Identify the preparation type.
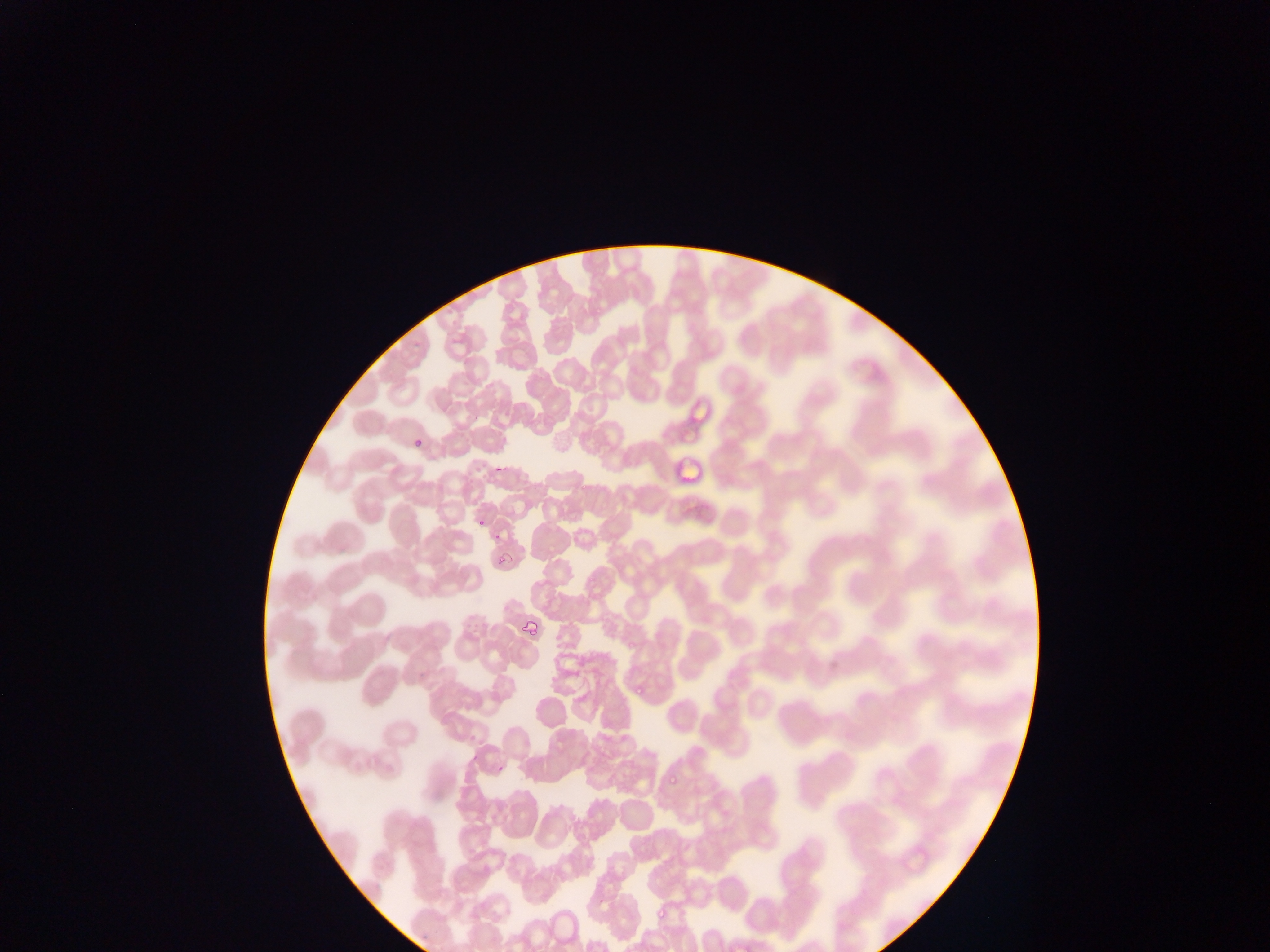
Thin blood film.

Approximate bounding boxes as [left, top, right, bottom] in pixels.
Summary:
  - Malaria parasite locations: [406, 433, 427, 452], [473, 515, 486, 532], [492, 546, 509, 567], [522, 616, 540, 640], [627, 681, 647, 694], [665, 775, 681, 787], [656, 902, 669, 921]
  - Leukocyte locations: [670, 448, 716, 492]
  - Field of view: single
  - Image size: 1270×952 pixels
  - Country: Ghana
  - Capture: mobile-phone photograph through a microscope